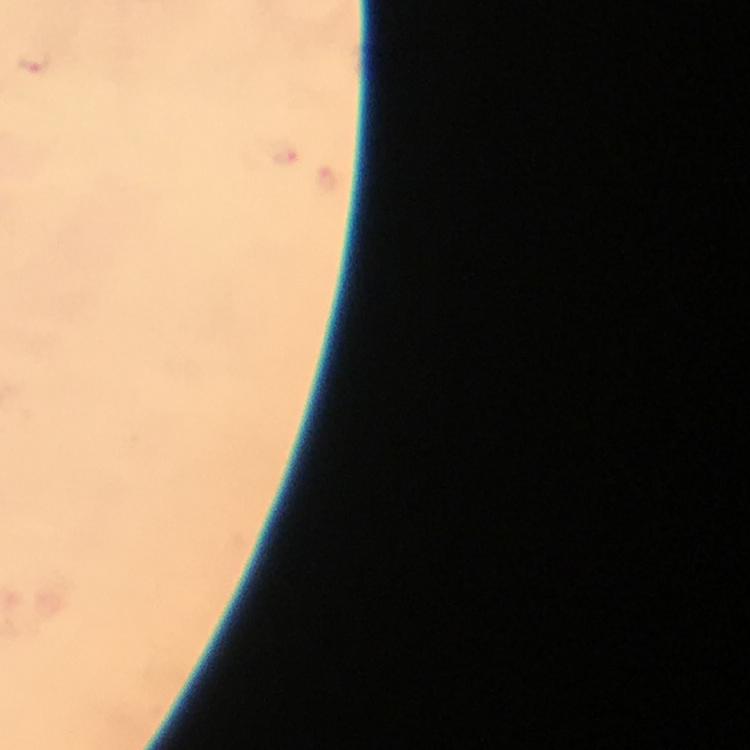
Approximate centers as {x, y} in pixels. Malaria parasite locations: {35, 61}, {285, 151}. Cropped region of a single field of view. Photographed through the microscope with a smartphone camera. Image is 750×750 pixels. 100x magnification. Thick smear. From a malaria diagnostic workup. Immersion oil applied. Giemsa-stained preparation.